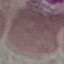

Malaria status: uninfected. Acquired by smartphone through the microscope eyepiece. Giemsa stain. Cell patch, automatically extracted from a larger field of view and resized to 64 × 64 pixels. Thin blood smear.